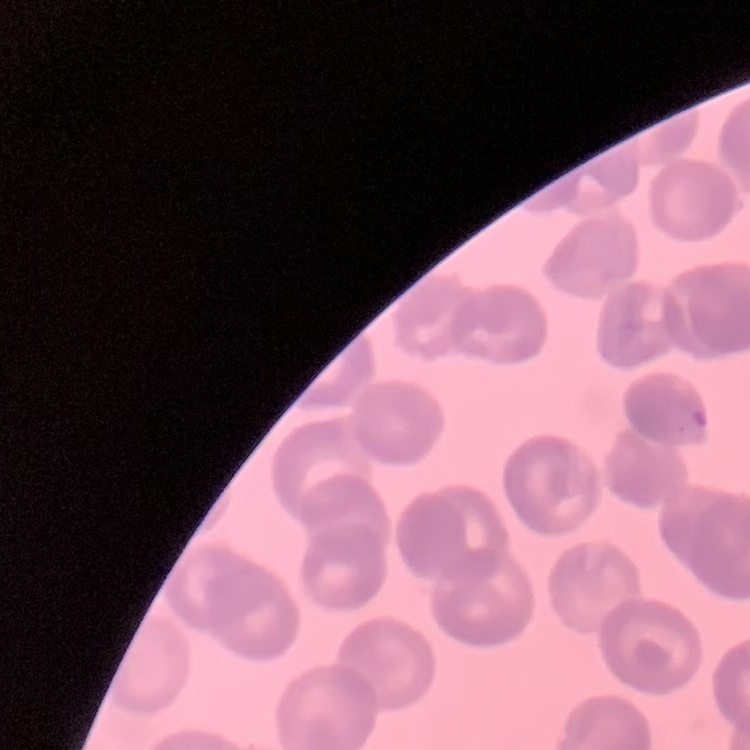
red blood cell morphology = rouleaux formation
stain = Field's or Giemsa
image type = square crop of a larger photomicrograph
preparation = thin peripheral smear